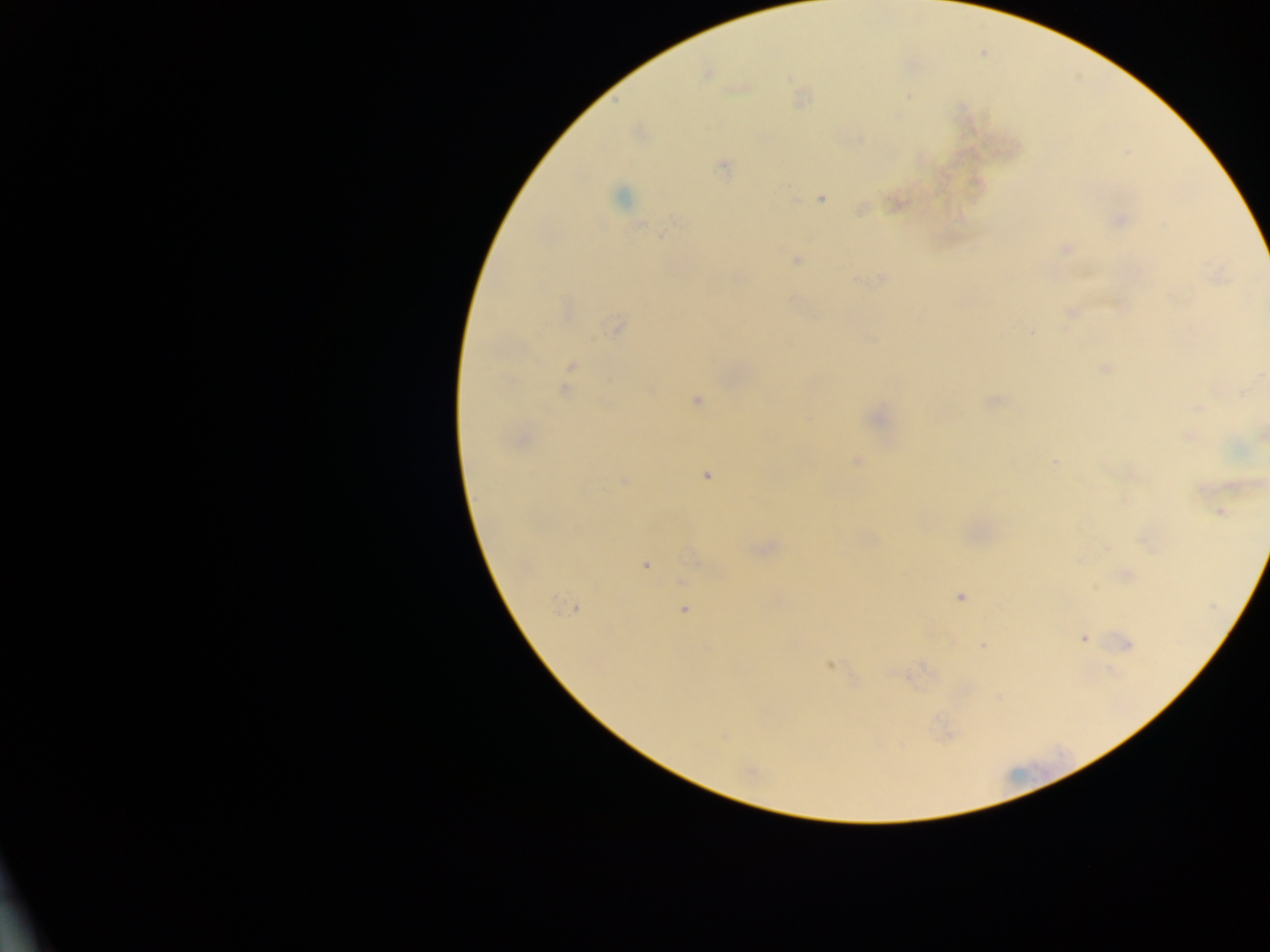
Approximate centers as (x, y) in pixels.
Summary:
  - Malaria parasite locations: (707, 74), (908, 96), (723, 167), (621, 197), (821, 198), (861, 210), (1120, 220), (676, 221), (641, 225), (1066, 248), (796, 260), (1216, 276), (739, 277), (882, 278), (856, 279), (1071, 312), (617, 327), (1031, 334), (572, 365), (1105, 367), (564, 391), (696, 400), (993, 400), (1200, 407), (877, 419), (1263, 435), (1188, 436), (520, 439), (858, 461), (1055, 461), (707, 476), (624, 481), (1234, 485), (1202, 488), (1221, 512), (1145, 543), (1106, 548), (763, 549), (646, 564), (1127, 575), (960, 596), (572, 608), (684, 611), (1083, 638), (1128, 644), (983, 646), (831, 665), (724, 737), (751, 770)
  - Preparation: thick blood smear
  - Image size: 1270×952 pixels
  - Field of view: single
  - Country: Ghana
  - Capture: mobile-phone photograph through a microscope